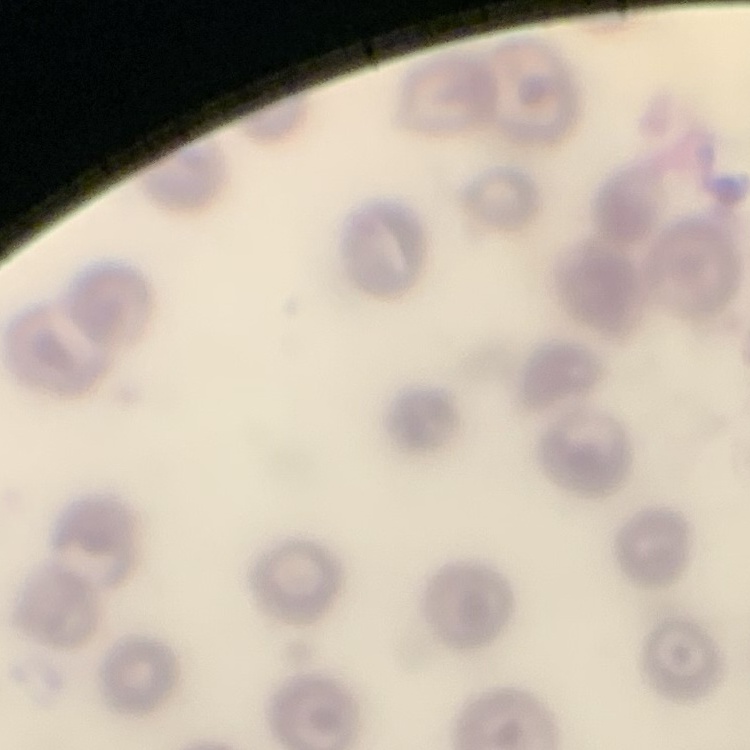

red blood cell morphology = no rouleaux formation
preparation = thin blood film
image type = square crop of a larger photomicrograph
stain = Field's or Giemsa